Outline each uninfected red blood cell.
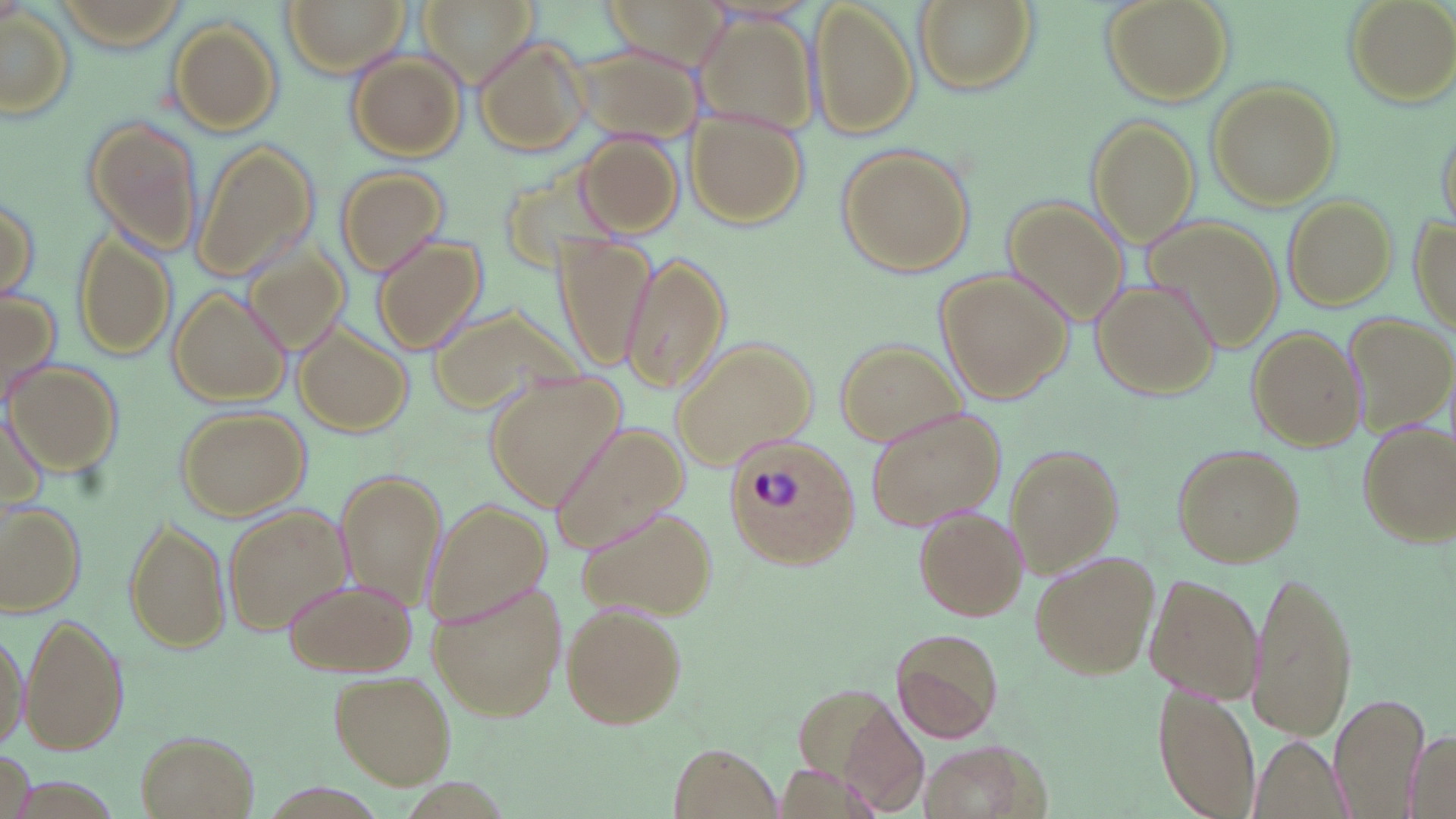

Approximate bounding boxes as named x1/y1/x2/y2 corners in pixels.
Uninfected red blood cells: (x1=281, y1=0, x2=410, y2=76), (x1=416, y1=0, x2=537, y2=83), (x1=603, y1=0, x2=728, y2=67), (x1=912, y1=0, x2=1040, y2=97), (x1=1102, y1=0, x2=1234, y2=106), (x1=1340, y1=0, x2=1455, y2=107), (x1=811, y1=1, x2=919, y2=139), (x1=0, y1=9, x2=77, y2=121), (x1=692, y1=10, x2=821, y2=138), (x1=166, y1=18, x2=284, y2=134), (x1=474, y1=35, x2=592, y2=155), (x1=573, y1=42, x2=704, y2=143), (x1=346, y1=51, x2=467, y2=161), (x1=1207, y1=82, x2=1340, y2=208), (x1=685, y1=107, x2=810, y2=231), (x1=1086, y1=115, x2=1200, y2=247), (x1=84, y1=116, x2=204, y2=254), (x1=1437, y1=120, x2=1455, y2=235), (x1=577, y1=130, x2=682, y2=237), (x1=190, y1=138, x2=318, y2=283), (x1=837, y1=146, x2=972, y2=276), (x1=499, y1=151, x2=621, y2=279), (x1=333, y1=165, x2=447, y2=277), (x1=0, y1=190, x2=42, y2=307), (x1=1283, y1=195, x2=1395, y2=310), (x1=1005, y1=197, x2=1132, y2=325), (x1=1413, y1=212, x2=1455, y2=333), (x1=1144, y1=219, x2=1283, y2=355), (x1=71, y1=227, x2=174, y2=361), (x1=553, y1=233, x2=657, y2=373), (x1=370, y1=234, x2=487, y2=355), (x1=245, y1=244, x2=351, y2=355), (x1=619, y1=251, x2=731, y2=395), (x1=937, y1=271, x2=1071, y2=403), (x1=1090, y1=280, x2=1221, y2=400), (x1=167, y1=288, x2=289, y2=407), (x1=0, y1=291, x2=62, y2=408), (x1=425, y1=300, x2=589, y2=421), (x1=1346, y1=310, x2=1455, y2=432), (x1=294, y1=323, x2=414, y2=437), (x1=1246, y1=325, x2=1364, y2=452), (x1=672, y1=338, x2=817, y2=464), (x1=835, y1=338, x2=964, y2=445), (x1=6, y1=359, x2=122, y2=476), (x1=487, y1=374, x2=625, y2=508), (x1=174, y1=405, x2=309, y2=520), (x1=1, y1=406, x2=50, y2=519), (x1=864, y1=406, x2=1007, y2=531), (x1=1355, y1=419, x2=1455, y2=546), (x1=546, y1=420, x2=690, y2=554), (x1=1004, y1=443, x2=1124, y2=576), (x1=1172, y1=443, x2=1305, y2=568), (x1=337, y1=470, x2=446, y2=615), (x1=424, y1=499, x2=552, y2=628), (x1=1, y1=502, x2=87, y2=617), (x1=220, y1=504, x2=351, y2=634), (x1=573, y1=505, x2=718, y2=619), (x1=916, y1=506, x2=1028, y2=622), (x1=122, y1=515, x2=230, y2=654), (x1=1029, y1=551, x2=1160, y2=682), (x1=1248, y1=569, x2=1358, y2=742), (x1=1146, y1=573, x2=1261, y2=703), (x1=282, y1=578, x2=415, y2=677), (x1=427, y1=580, x2=569, y2=721), (x1=559, y1=601, x2=690, y2=731), (x1=20, y1=613, x2=131, y2=757), (x1=0, y1=622, x2=28, y2=755), (x1=890, y1=625, x2=1006, y2=744), (x1=330, y1=671, x2=455, y2=788), (x1=792, y1=684, x2=932, y2=816), (x1=1151, y1=685, x2=1263, y2=819), (x1=1330, y1=692, x2=1428, y2=817), (x1=1401, y1=730, x2=1455, y2=819), (x1=136, y1=731, x2=257, y2=819), (x1=1248, y1=734, x2=1349, y2=819), (x1=916, y1=740, x2=1038, y2=819), (x1=667, y1=743, x2=786, y2=819), (x1=3, y1=747, x2=34, y2=819).

Plasmodium ovale-infected red blood cell locations: (x1=725, y1=435, x2=860, y2=570). Slide-level diagnosis: Plasmodium ovale. Image is 1456×819 pixels. Optical microscopy. 1000x magnification. One field of a larger specimen. May-Grünwald-Giemsa-stained preparation. Thin blood film.